Classify this cell by malaria status.
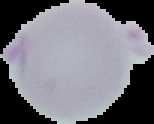

Uninfected.

preparation = thin blood smear
image type = cell region segmented out of the field of view; surrounding area masked to black
image size = 154×124 pixels